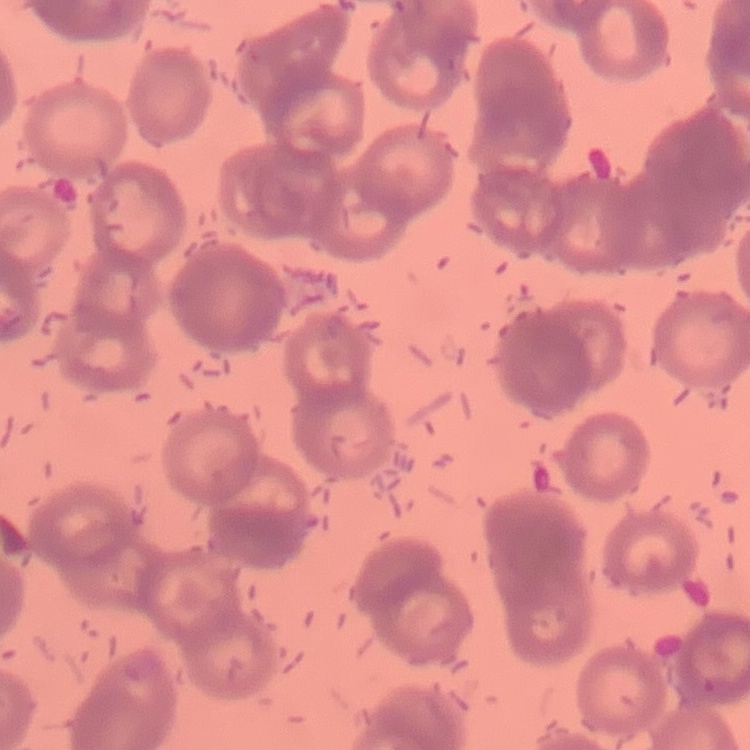

Summary:
  - Red blood cell morphology: rouleaux formation
  - Stain: Field's or Giemsa
  - Image type: square crop of a larger photomicrograph
  - Preparation: thin blood smear